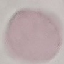

malaria status = uninfected
preparation = thin blood film
capture = smartphone through the microscope eyepiece
stain = Giemsa
image type = automatically extracted cell patch, resized to 64 × 64 pixels